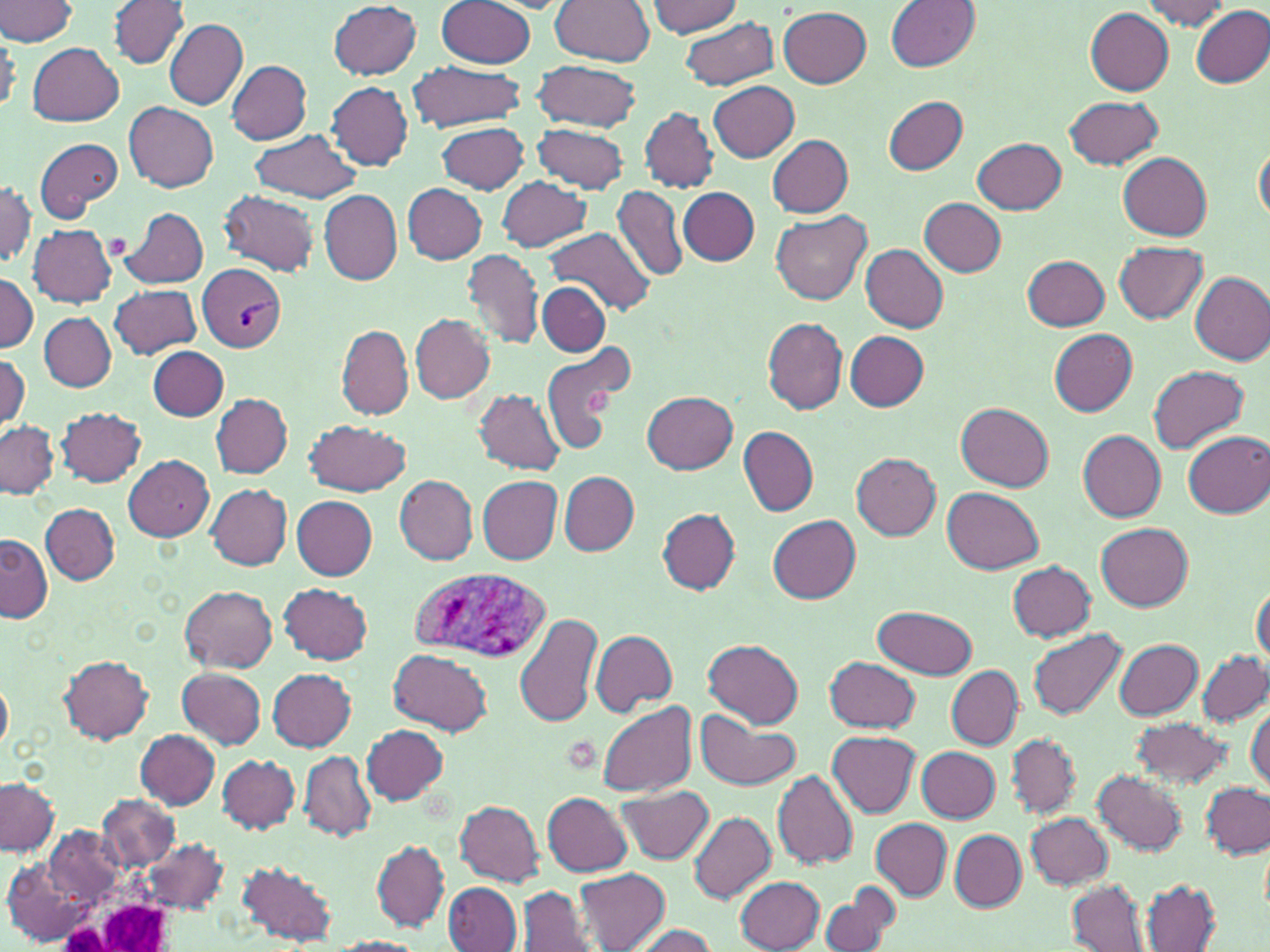
{
  "slide_level_diagnosis": "Plasmodium vivax",
  "image_size": "1270×952 pixels",
  "field_of_view": "single",
  "uninfected_red_blood_cell_locations": "approximate bounding boxes as (x1, y1, x2, y2) in pixels: (0, 0, 79, 46), (434, 0, 537, 68), (549, 0, 656, 65), (1140, 0, 1234, 31), (109, 1, 190, 70), (329, 1, 423, 79), (648, 1, 743, 37), (885, 1, 978, 71), (1190, 6, 1270, 89), (779, 7, 873, 88), (1086, 8, 1175, 95), (678, 16, 778, 90), (165, 20, 247, 109), (27, 43, 124, 126), (227, 59, 312, 143), (531, 60, 641, 132), (405, 63, 529, 131), (709, 81, 800, 163), (327, 83, 414, 170), (883, 95, 968, 175), (1064, 95, 1163, 169), (123, 101, 219, 192), (640, 107, 718, 192), (436, 121, 529, 195), (531, 123, 630, 193), (249, 130, 362, 203), (768, 135, 852, 217), (35, 137, 121, 222), (973, 137, 1068, 213), (1254, 140, 1270, 224), (1120, 152, 1212, 240), (497, 176, 590, 253), (1, 179, 36, 269), (403, 185, 487, 263), (611, 185, 687, 281), (680, 188, 759, 266), (216, 189, 320, 276), (318, 189, 402, 284), (918, 197, 1007, 276), (118, 206, 210, 289), (772, 210, 872, 305), (27, 225, 117, 307), (545, 227, 656, 314), (1113, 242, 1208, 324), (860, 245, 949, 332), (462, 248, 544, 351), (1024, 256, 1111, 330), (0, 271, 37, 353), (1190, 271, 1270, 366), (538, 283, 611, 356), (110, 284, 202, 359), (40, 312, 114, 391), (410, 313, 494, 403), (762, 317, 848, 415), (337, 324, 414, 418), (1048, 327, 1139, 416), (844, 331, 929, 409), (537, 338, 638, 455), (149, 347, 228, 421), (1, 351, 29, 429), (1148, 365, 1249, 453), (474, 389, 564, 475), (643, 392, 739, 474), (209, 393, 293, 476), (957, 403, 1055, 492), (56, 407, 146, 487), (305, 419, 412, 497), (0, 420, 59, 499), (739, 426, 817, 517), (1077, 430, 1166, 521), (1183, 430, 1270, 518), (851, 453, 941, 540), (124, 456, 213, 541), (560, 471, 640, 555), (393, 474, 478, 565), (477, 476, 562, 563), (206, 484, 292, 571), (943, 487, 1043, 574), (292, 496, 378, 579), (42, 504, 118, 584), (659, 508, 740, 593), (769, 515, 860, 603), (1095, 523, 1193, 611), (1, 534, 51, 622), (1007, 561, 1097, 642), (279, 583, 373, 664), (179, 585, 277, 673), (1251, 585, 1269, 665), (873, 606, 978, 679), (516, 613, 602, 730), (1027, 628, 1127, 721), (590, 630, 678, 716), (704, 639, 804, 728), (1113, 639, 1201, 718), (390, 649, 491, 734), (1197, 650, 1270, 726), (59, 656, 153, 743), (825, 656, 920, 732), (946, 666, 1022, 749), (268, 668, 356, 751), (175, 669, 266, 748), (0, 676, 14, 755), (597, 701, 697, 797), (1247, 703, 1269, 791), (697, 711, 800, 787), (1129, 717, 1233, 787), (361, 724, 449, 805), (136, 729, 219, 809), (827, 731, 920, 816), (1007, 735, 1078, 816), (916, 745, 999, 823), (299, 751, 376, 842), (218, 754, 300, 834), (773, 770, 859, 869), (1092, 770, 1185, 855), (1072, 775, 1174, 916), (0, 779, 58, 856), (1201, 783, 1268, 858), (616, 785, 714, 864), (543, 792, 632, 875), (99, 793, 179, 870), (455, 800, 545, 887), (687, 812, 777, 904), (1027, 813, 1113, 889), (871, 820, 951, 900), (47, 826, 122, 903), (950, 830, 1026, 910), (144, 838, 226, 912), (372, 840, 449, 931), (236, 860, 338, 947), (3, 861, 89, 946), (575, 869, 669, 951), (737, 877, 824, 952), (1142, 879, 1220, 950), (1067, 881, 1149, 951), (444, 882, 522, 951), (819, 885, 901, 952), (518, 887, 593, 952), (629, 923, 718, 952), (328, 937, 427, 952)",
  "platelet_locations": "approximate bounding boxes as (x1, y1, x2, y2) in pixels: (585, 385, 620, 416)",
  "white_blood_cell_locations": "approximate bounding boxes as (x1, y1, x2, y2) in pixels: (52, 873, 180, 950)",
  "modality": "light microscopy",
  "stain": "May-Grünwald-Giemsa",
  "plasmodium_vivax_infected_red_blood_cell_locations": "approximate bounding boxes as (x1, y1, x2, y2) in pixels: (197, 265, 288, 353), (409, 567, 551, 664)",
  "preparation": "thin blood film",
  "magnification": "1000x"
}